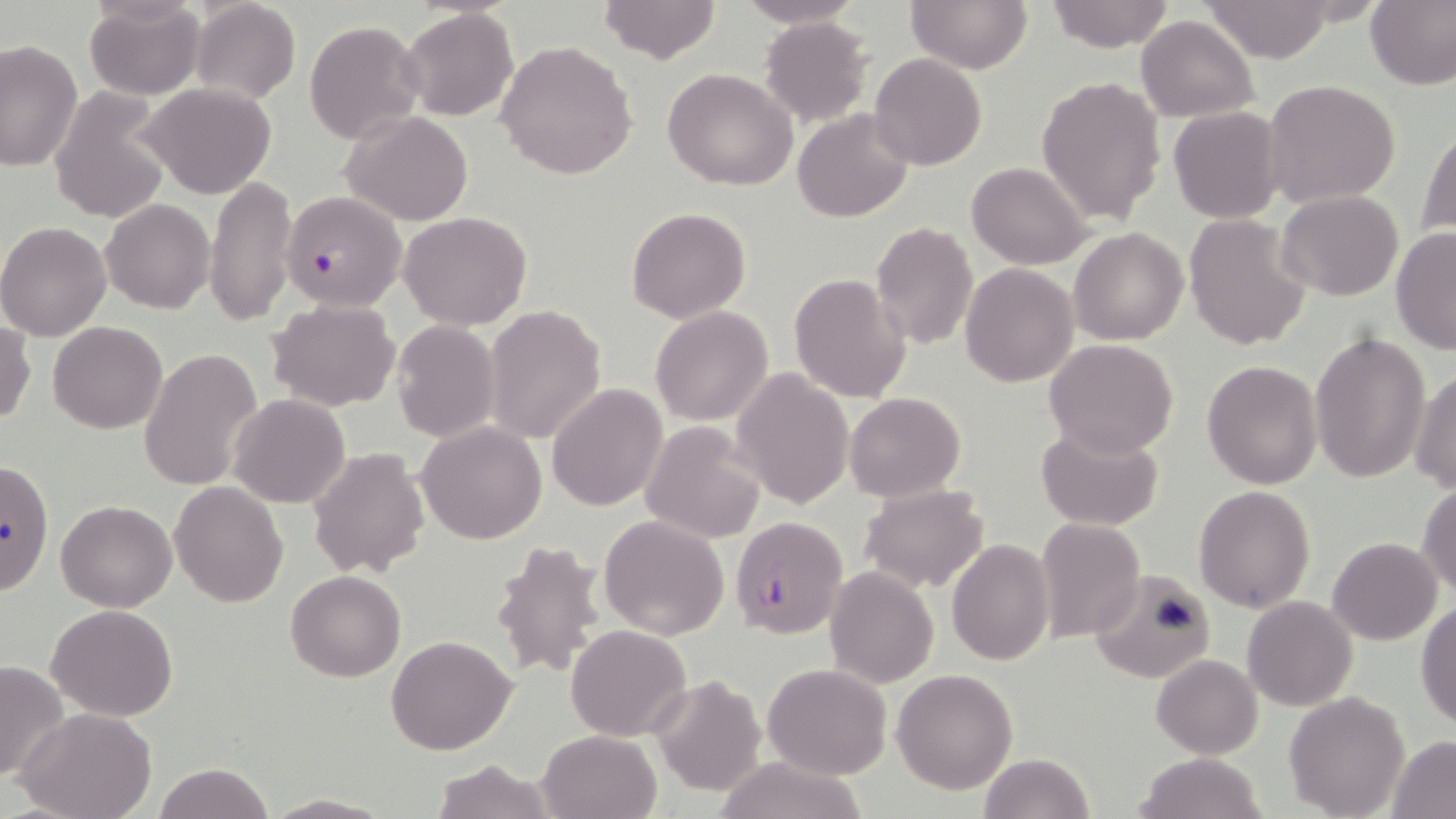
{
  "slide_level_diagnosis": "Plasmodium falciparum",
  "preparation": "thin blood film",
  "field_of_view": "one of a larger specimen",
  "magnification": "1000x",
  "uninfected_red_blood_cell_locations": "approximate bounding boxes as (x1, y1, x2, y2) in pixels: (597, 0, 722, 62), (736, 0, 864, 29), (905, 0, 1033, 73), (1042, 0, 1177, 52), (1365, 0, 1456, 91), (83, 1, 205, 100), (189, 1, 301, 104), (1202, 1, 1336, 64), (401, 8, 517, 122), (1136, 14, 1258, 121), (759, 16, 872, 126), (304, 19, 425, 143), (0, 39, 82, 174), (496, 40, 638, 180), (869, 53, 988, 170), (663, 68, 800, 190), (1036, 75, 1166, 226), (1263, 79, 1403, 210), (139, 81, 278, 199), (46, 90, 172, 221), (1168, 107, 1284, 222), (792, 108, 912, 223), (344, 112, 473, 225), (1418, 122, 1455, 243), (967, 162, 1090, 269), (205, 176, 297, 327), (1277, 190, 1403, 301), (101, 199, 214, 313), (626, 208, 750, 322), (399, 211, 532, 331), (1185, 215, 1311, 351), (0, 221, 112, 342), (869, 222, 978, 352), (1069, 227, 1189, 345), (1390, 228, 1456, 354), (960, 262, 1078, 387), (788, 272, 912, 405), (268, 298, 401, 411), (482, 305, 607, 443), (650, 307, 774, 425), (0, 320, 36, 427), (48, 320, 168, 434), (391, 321, 500, 441), (1309, 331, 1431, 484), (1045, 339, 1178, 457), (140, 347, 262, 492), (1202, 360, 1323, 488), (732, 368, 854, 509), (1410, 370, 1456, 492), (547, 383, 667, 513), (845, 393, 965, 502), (229, 394, 348, 508), (640, 421, 767, 542), (416, 422, 548, 545), (1035, 423, 1165, 530), (308, 445, 431, 581), (0, 458, 51, 591), (170, 481, 287, 607), (1416, 482, 1456, 599), (859, 485, 987, 592), (1193, 485, 1316, 612), (57, 500, 178, 612), (599, 516, 730, 640), (1035, 517, 1145, 644), (1327, 536, 1443, 644), (489, 537, 610, 683), (947, 538, 1055, 665), (825, 567, 939, 687), (1088, 567, 1218, 684), (285, 570, 405, 682), (1242, 596, 1357, 710), (1416, 599, 1456, 731), (47, 604, 179, 721), (566, 624, 692, 742), (386, 636, 516, 756), (1151, 653, 1263, 759), (0, 660, 69, 782), (762, 663, 893, 780), (892, 669, 1017, 793), (649, 677, 767, 798), (1284, 692, 1411, 817), (16, 708, 158, 819), (538, 729, 659, 818), (1387, 734, 1456, 817), (1136, 752, 1266, 819), (979, 753, 1094, 819), (711, 756, 871, 819), (428, 759, 559, 819), (151, 763, 274, 819), (263, 793, 394, 818)",
  "modality": "optical microscopy",
  "image_size": "1456×819 pixels",
  "plasmodium_falciparum_infected_red_blood_cell_locations": "approximate bounding boxes as (x1, y1, x2, y2) in pixels: (282, 191, 405, 312), (729, 516, 846, 639)",
  "stain": "May-Grünwald-Giemsa"
}